Name the blood parasite species.
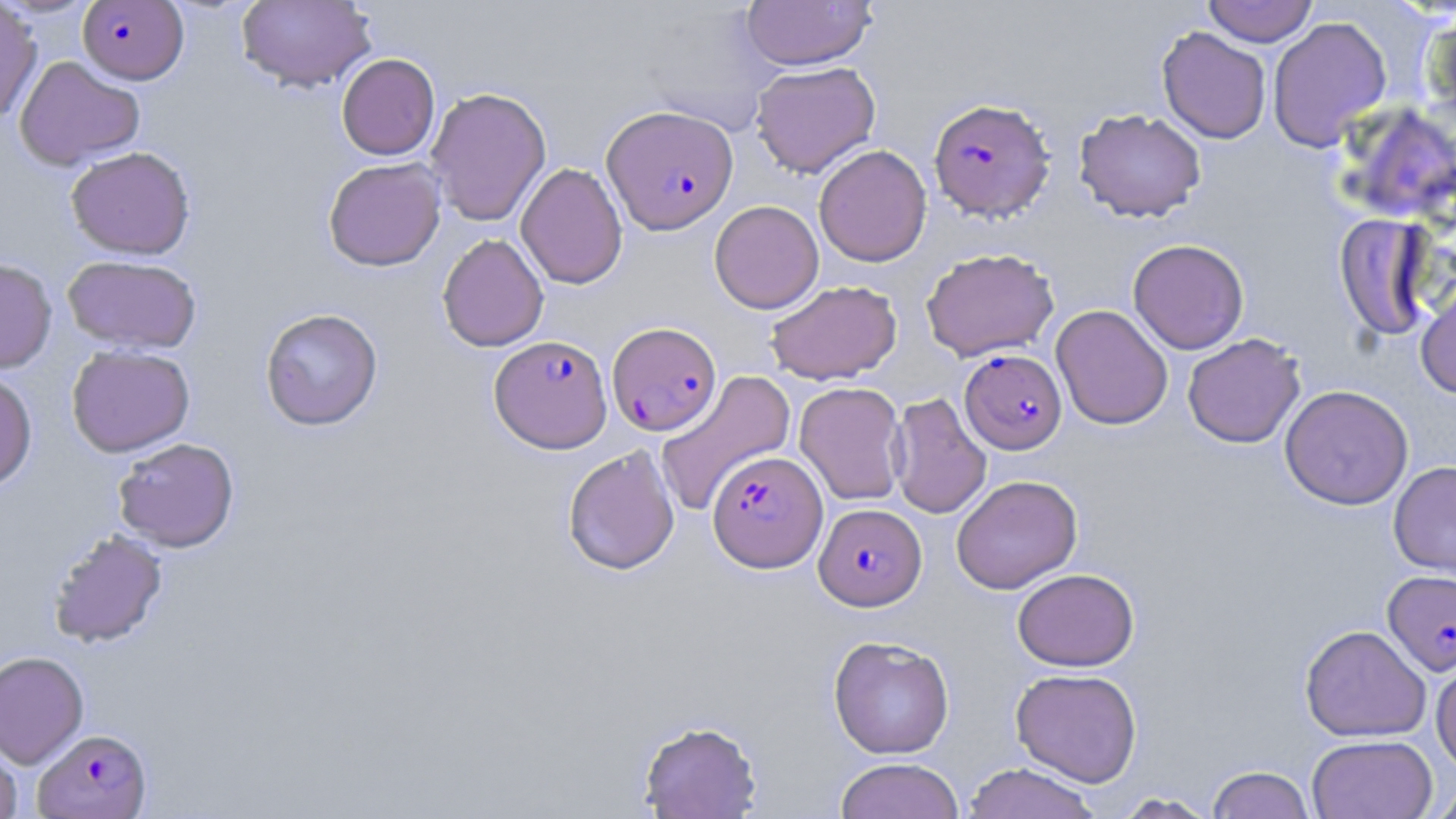

Plasmodium falciparum.

{
  "field_of_view": "single",
  "magnification": "1000x",
  "stain": "May-Grünwald-Giemsa",
  "modality": "light microscopy",
  "uninfected_red_blood_cell_locations": "approximate bounding boxes as named x1/y1/x2/y2 corners in pixels: (x1=0, y1=0, x2=42, y2=123), (x1=236, y1=0, x2=376, y2=93), (x1=1203, y1=0, x2=1318, y2=47), (x1=740, y1=1, x2=877, y2=70), (x1=1267, y1=17, x2=1392, y2=152), (x1=1157, y1=26, x2=1271, y2=144), (x1=336, y1=53, x2=440, y2=160), (x1=14, y1=54, x2=145, y2=171), (x1=750, y1=61, x2=881, y2=178), (x1=425, y1=87, x2=551, y2=227), (x1=1338, y1=101, x2=1456, y2=227), (x1=1073, y1=108, x2=1207, y2=222), (x1=65, y1=145, x2=195, y2=260), (x1=813, y1=145, x2=932, y2=267), (x1=323, y1=157, x2=446, y2=271), (x1=515, y1=162, x2=628, y2=289), (x1=709, y1=200, x2=824, y2=314), (x1=1334, y1=213, x2=1437, y2=341), (x1=437, y1=233, x2=549, y2=352), (x1=1127, y1=239, x2=1249, y2=354), (x1=921, y1=247, x2=1060, y2=362), (x1=62, y1=255, x2=201, y2=354), (x1=0, y1=258, x2=57, y2=374), (x1=765, y1=280, x2=902, y2=385), (x1=1415, y1=281, x2=1456, y2=399), (x1=1051, y1=304, x2=1174, y2=430), (x1=260, y1=307, x2=383, y2=431), (x1=1182, y1=334, x2=1306, y2=448), (x1=66, y1=345, x2=196, y2=457), (x1=0, y1=370, x2=37, y2=492), (x1=655, y1=372, x2=798, y2=521), (x1=794, y1=382, x2=907, y2=506), (x1=1279, y1=385, x2=1414, y2=510), (x1=887, y1=393, x2=991, y2=520), (x1=113, y1=437, x2=240, y2=552), (x1=563, y1=444, x2=680, y2=576), (x1=1388, y1=461, x2=1456, y2=580), (x1=951, y1=475, x2=1082, y2=594), (x1=47, y1=528, x2=168, y2=648), (x1=1012, y1=568, x2=1139, y2=671), (x1=1300, y1=624, x2=1432, y2=742), (x1=828, y1=635, x2=955, y2=759), (x1=0, y1=650, x2=89, y2=768), (x1=1431, y1=650, x2=1456, y2=776), (x1=1010, y1=668, x2=1142, y2=786), (x1=637, y1=718, x2=763, y2=818), (x1=1307, y1=734, x2=1438, y2=819), (x1=0, y1=739, x2=22, y2=819), (x1=835, y1=757, x2=965, y2=819), (x1=962, y1=763, x2=1101, y2=819), (x1=1206, y1=765, x2=1315, y2=819), (x1=1429, y1=782, x2=1456, y2=819), (x1=1111, y1=792, x2=1220, y2=818)",
  "image_size": "1456×819 pixels",
  "plasmodium_falciparum_infected_red_blood_cell_locations": "approximate bounding boxes as named x1/y1/x2/y2 corners in pixels: (x1=77, y1=1, x2=188, y2=84), (x1=929, y1=97, x2=1055, y2=221), (x1=602, y1=105, x2=738, y2=234), (x1=607, y1=321, x2=722, y2=436), (x1=490, y1=335, x2=613, y2=453), (x1=960, y1=349, x2=1067, y2=454), (x1=707, y1=451, x2=828, y2=572), (x1=815, y1=504, x2=926, y2=611), (x1=1382, y1=570, x2=1456, y2=676), (x1=33, y1=728, x2=152, y2=818)",
  "preparation": "thin blood film"
}